Outline each Plasmodium ovale-infected red blood cell.
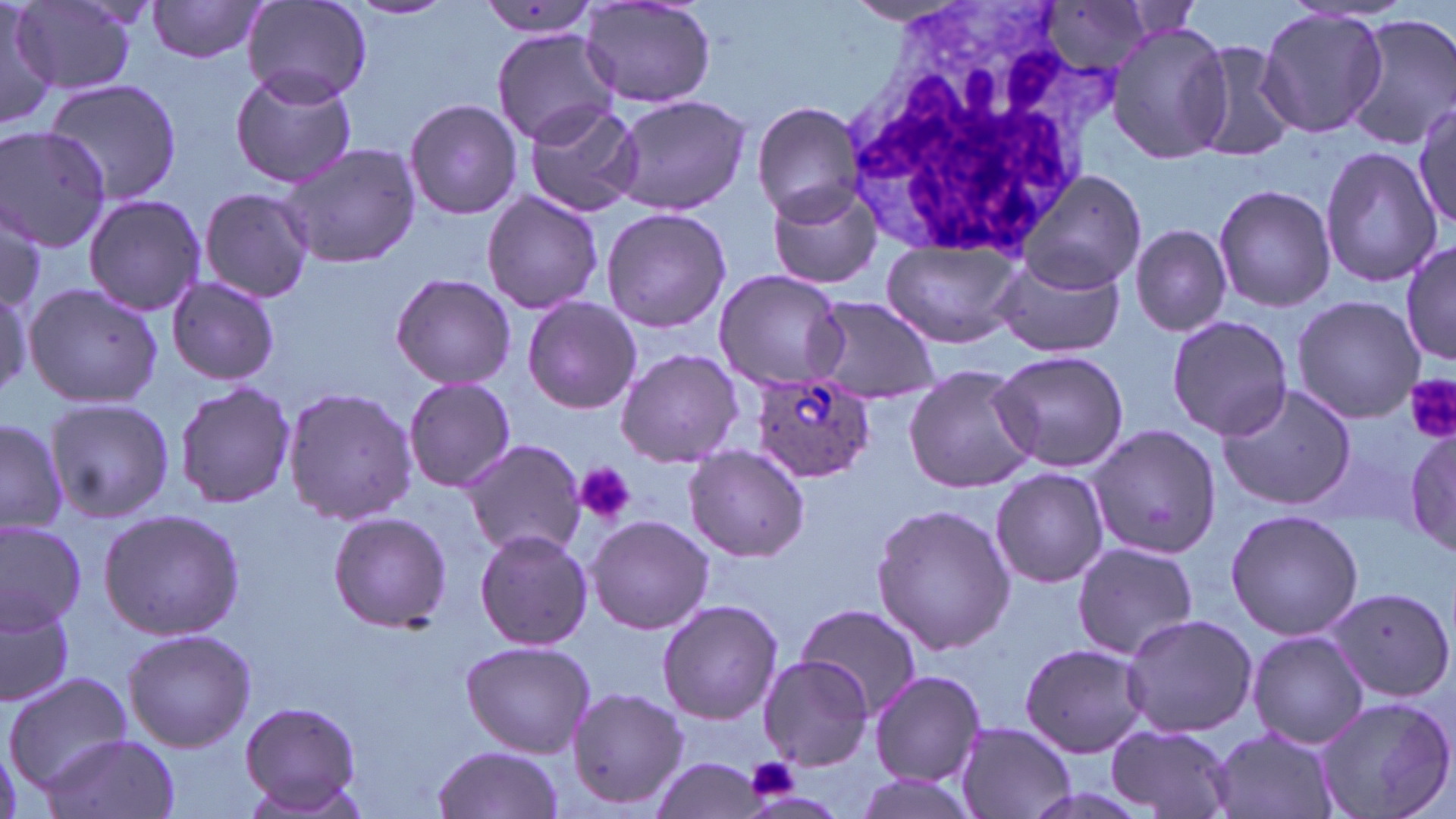
Approximate bounding boxes as [x1, y1, x2, y2] in pixels.
Plasmodium ovale-infected red blood cells: [749, 368, 874, 482].

{
  "slide_level_diagnosis": "Plasmodium ovale",
  "modality": "optical microscopy",
  "preparation": "thin blood film",
  "stain": "May-Grünwald-Giemsa",
  "image_size": "1456×819 pixels",
  "platelet_locations": "approximate bounding boxes as [x1, y1, x2, y2] in pixels: [1404, 373, 1456, 442], [573, 462, 636, 526], [745, 756, 800, 801]",
  "uninfected_red_blood_cell_locations": "approximate bounding boxes as [x1, y1, x2, y2] in pixels: [346, 0, 458, 21], [0, 1, 57, 129], [15, 1, 138, 96], [146, 1, 267, 64], [242, 2, 373, 105], [581, 2, 717, 110], [843, 2, 965, 26], [475, 3, 603, 40], [1041, 3, 1159, 74], [1256, 10, 1389, 139], [1346, 14, 1455, 149], [1108, 22, 1232, 164], [492, 27, 621, 148], [1186, 40, 1303, 165], [228, 68, 358, 189], [43, 78, 183, 207], [611, 94, 749, 216], [404, 97, 523, 221], [1412, 100, 1456, 233], [753, 101, 866, 222], [523, 102, 645, 219], [0, 125, 112, 250], [278, 140, 421, 269], [1318, 146, 1440, 288], [1016, 168, 1146, 294], [766, 177, 886, 292], [1213, 184, 1336, 314], [199, 188, 315, 303], [481, 190, 603, 314], [83, 192, 208, 316], [600, 206, 732, 333], [0, 207, 47, 308], [1130, 222, 1232, 337], [880, 236, 1024, 349], [1402, 239, 1456, 368], [989, 253, 1128, 359], [712, 269, 846, 391], [390, 271, 516, 389], [166, 276, 280, 385], [22, 282, 163, 411], [0, 285, 33, 403], [805, 295, 942, 403], [522, 296, 642, 415], [1292, 296, 1425, 423], [1166, 314, 1293, 442], [615, 349, 743, 467], [987, 349, 1133, 473], [902, 365, 1039, 494], [403, 375, 516, 492], [173, 382, 297, 508], [1218, 384, 1357, 512], [282, 386, 417, 529], [42, 395, 175, 524], [0, 415, 69, 535], [1086, 424, 1221, 560], [1402, 424, 1456, 555], [461, 439, 588, 561], [684, 445, 809, 563], [991, 467, 1109, 589], [871, 503, 1016, 656], [98, 507, 246, 641], [1226, 508, 1362, 642], [326, 511, 449, 630], [586, 515, 713, 635], [0, 522, 86, 629], [474, 528, 592, 650], [1069, 542, 1200, 660], [1329, 584, 1455, 703], [0, 590, 74, 710], [656, 599, 782, 724], [795, 603, 920, 718], [1121, 611, 1258, 739], [121, 628, 257, 752], [1247, 630, 1367, 750], [460, 641, 594, 757], [1018, 643, 1150, 757], [758, 654, 874, 770], [868, 669, 986, 787], [4, 672, 132, 789], [567, 686, 690, 810], [1312, 694, 1454, 819], [238, 701, 365, 814], [955, 721, 1077, 819], [1105, 724, 1237, 819], [1208, 727, 1342, 819], [38, 734, 181, 819], [430, 744, 564, 819], [651, 756, 766, 819], [857, 773, 985, 819]",
  "white_blood_cell_locations": "approximate bounding boxes as [x1, y1, x2, y2] in pixels: [849, 10, 1105, 258]",
  "magnification": "1000x",
  "field_of_view": "single"
}